Assess this cell for malaria.
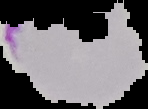

Parasitized.

image_type: segmented cell region on a black background
preparation: thin blood film
image_size: 148×109 pixels